Assess this cell for malaria.
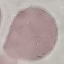
It is uninfected.

stain: Giemsa
image_type: cell patch, automatically extracted from a larger field of view and resized to 64 × 64 pixels
preparation: thin blood smear
capture: smartphone camera at the microscope eyepiece